State the preparation type.
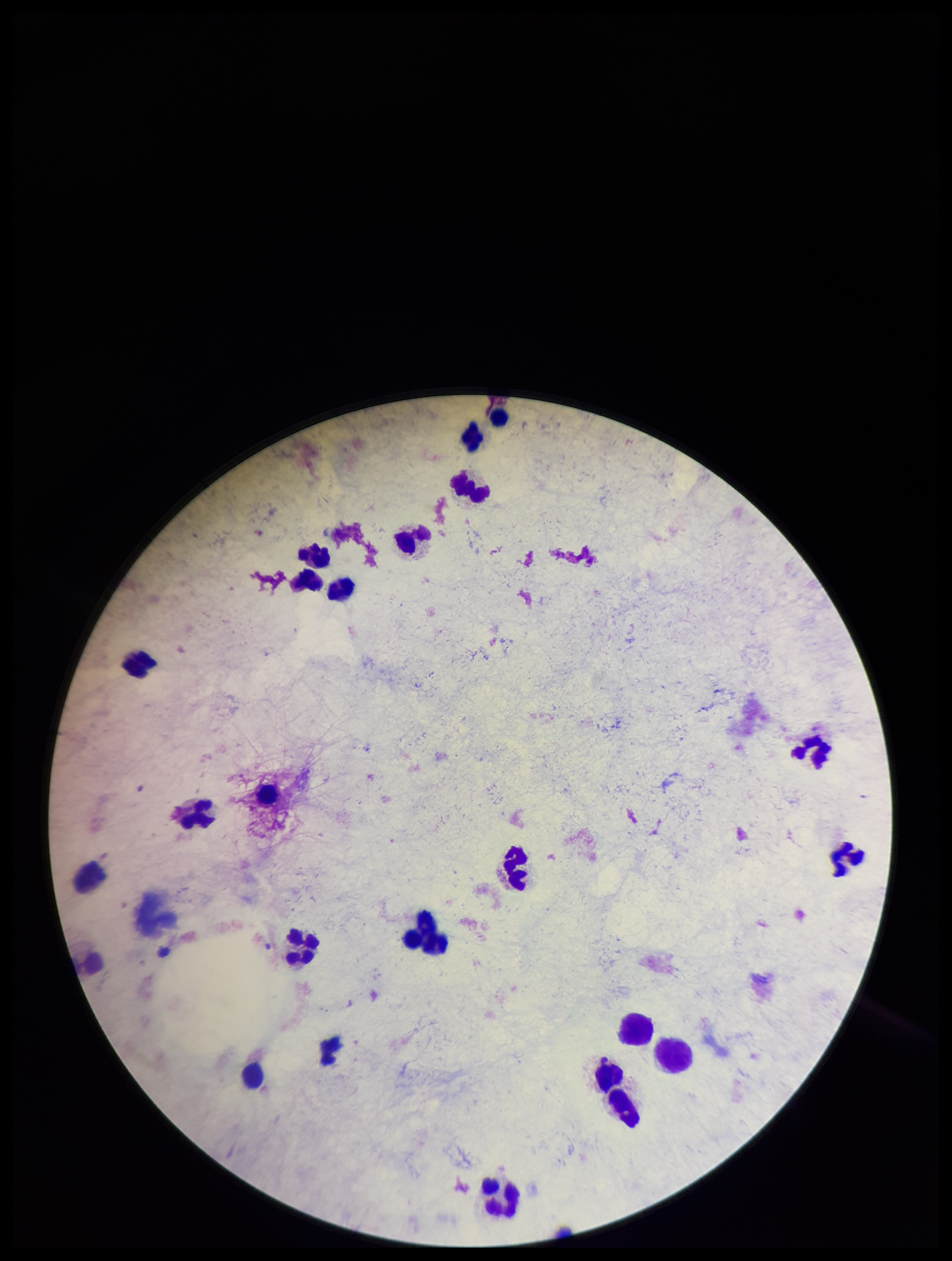
It is a thick blood smear.

capture = smartphone photograph through the microscope eyepiece
Plasmodium parasites = none identified
image size = 952×1261 pixels
parasite count = 0
field of view = single
leukocyte count = 22
patient malaria status = negative
stain = Giemsa